State which parasite is depicted.
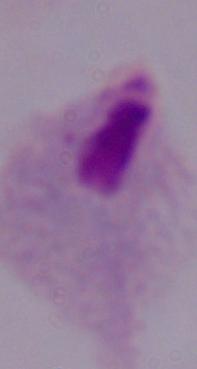
A trichomonad.

Summary:
  - Modality: micrograph
  - Magnification: 1000x